Point out each Plasmodium parasite.
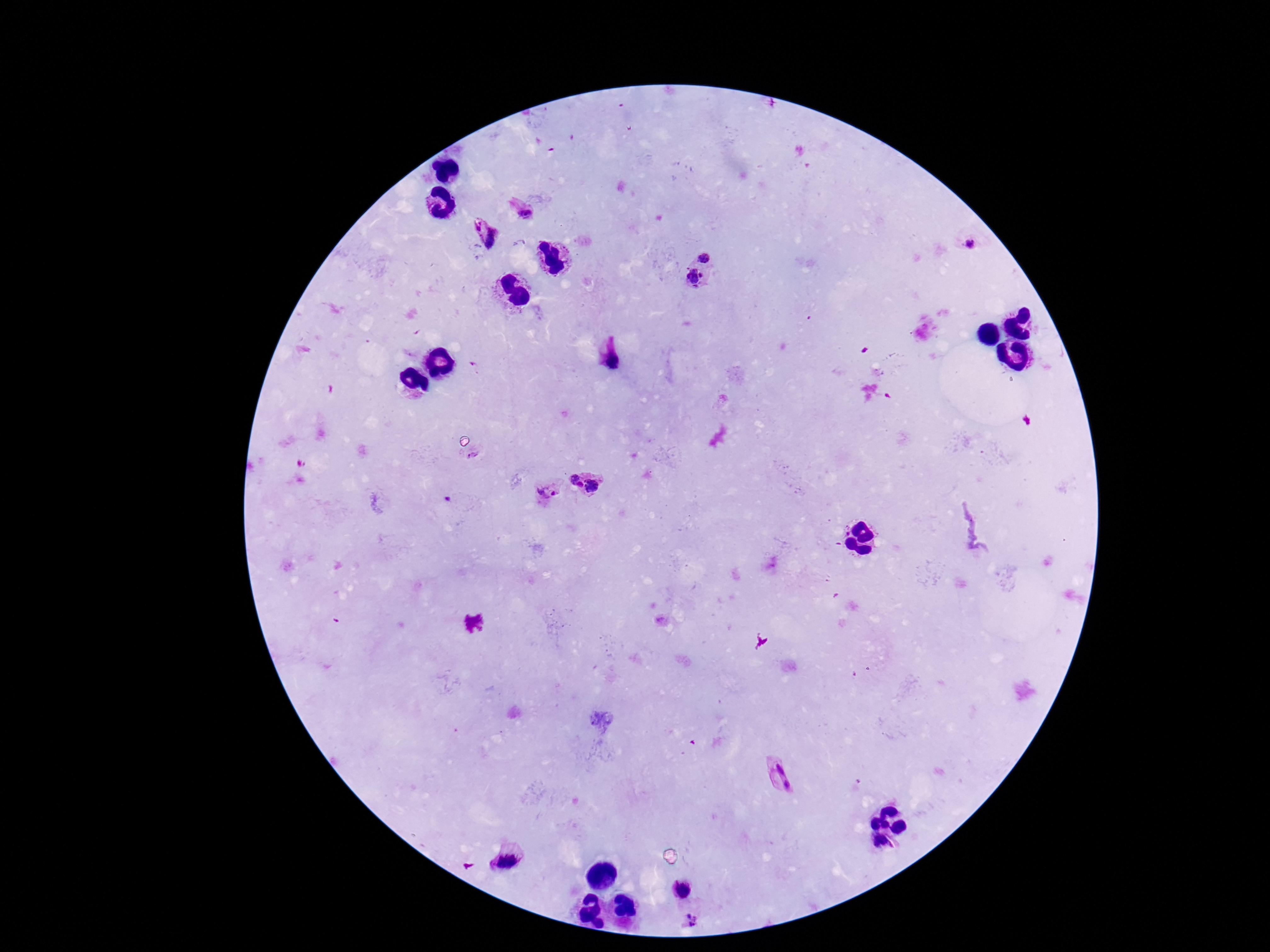

Approximate centers as [x, y] in pixels.
Plasmodium parasites: [524, 213], [477, 225], [494, 241], [970, 244], [706, 254], [694, 277], [614, 360], [473, 456], [574, 477], [580, 485], [594, 487], [542, 492], [554, 493], [448, 499], [779, 768], [787, 785], [507, 862], [682, 889], [688, 916], [696, 919], [689, 924], [694, 924].

Summary:
  - Stain: Giemsa
  - Field of view: single
  - Image size: 1270×952 pixels
  - Patient malaria status: infected
  - Preparation: thick blood smear
  - Capture: smartphone camera through the microscope eyepiece
  - Magnification: 100x